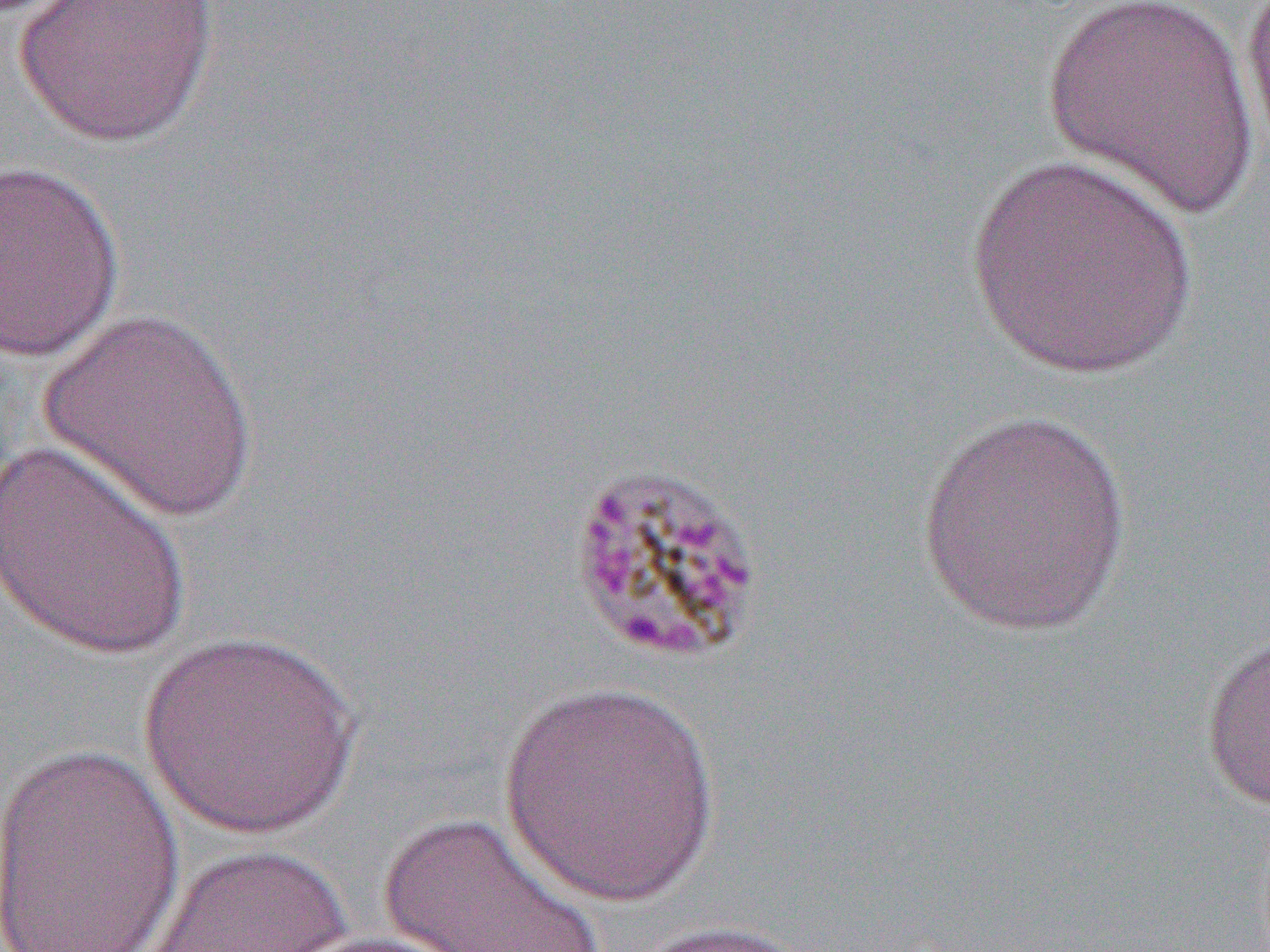

Summary:
  - Coordinate format: approximate bounding boxes as [x1, y1, x2, y2] in pixels
  - Uninfected red blood cell locations: [14, 0, 219, 147], [1042, 0, 1262, 220], [1239, 0, 1270, 168], [967, 152, 1199, 382], [0, 159, 126, 364], [36, 306, 262, 526], [917, 405, 1134, 638], [0, 438, 196, 663], [1200, 626, 1270, 810], [140, 630, 363, 839], [496, 678, 724, 912], [1, 740, 187, 951], [378, 810, 609, 952], [139, 844, 361, 952], [622, 918, 819, 951], [284, 930, 471, 952]
  - Slide-level diagnosis: Plasmodium malariae
  - Modality: light microscopy
  - Preparation: thin blood smear
  - Magnification: 1000x
  - Field of view: single
  - Image size: 1270×952 pixels